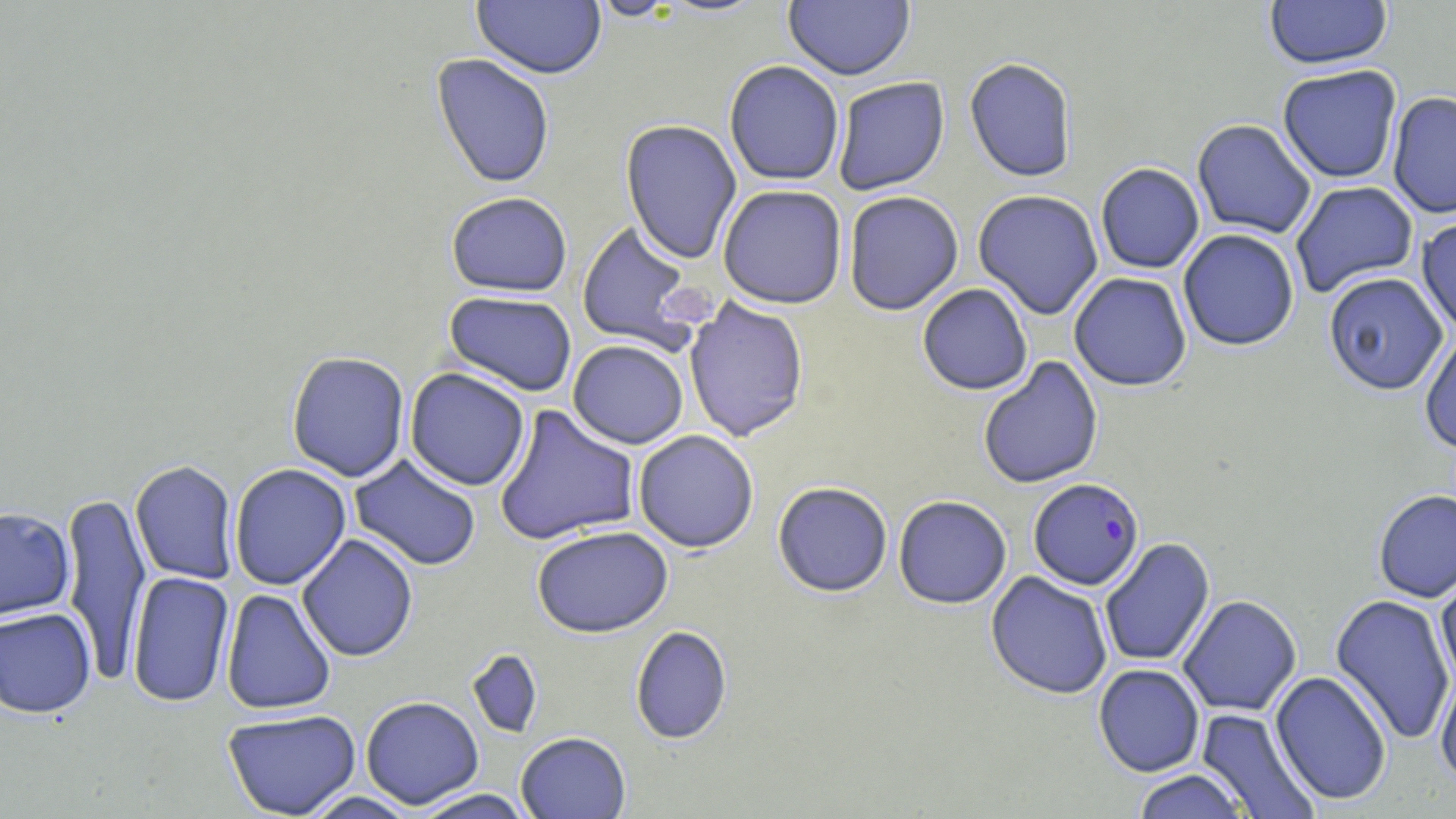

Summary:
  - Coordinate format: approximate bounding boxes as (x1, y1, x2, y2) in pixels
  - Uninfected red blood cell locations: (471, 0, 607, 79), (586, 0, 685, 21), (1264, 0, 1393, 71), (783, 1, 915, 81), (431, 53, 555, 189), (964, 57, 1078, 182), (724, 60, 845, 186), (1277, 64, 1403, 184), (832, 76, 950, 196), (1387, 90, 1456, 219), (620, 119, 742, 264), (1192, 119, 1317, 239), (1095, 162, 1205, 274), (1290, 180, 1419, 298), (717, 184, 847, 309), (972, 189, 1104, 319), (843, 191, 964, 315), (445, 192, 573, 297), (1416, 214, 1456, 338), (575, 221, 703, 354), (1177, 228, 1300, 351), (1323, 271, 1449, 396), (1068, 272, 1192, 392), (917, 283, 1033, 395), (443, 290, 578, 396), (683, 296, 810, 443), (1419, 332, 1456, 453), (568, 340, 689, 449), (286, 351, 410, 482), (977, 356, 1103, 490), (405, 368, 530, 491), (493, 404, 640, 546), (633, 430, 759, 553), (349, 454, 483, 571), (130, 460, 239, 585), (229, 463, 351, 590), (772, 482, 893, 597), (59, 489, 151, 683), (1373, 489, 1456, 602), (893, 495, 1012, 609), (0, 505, 75, 625), (532, 525, 673, 638), (296, 534, 419, 662), (1099, 537, 1215, 668), (1435, 569, 1456, 690), (985, 570, 1113, 699), (126, 571, 235, 708), (220, 588, 337, 715), (1177, 594, 1302, 716), (1329, 594, 1455, 744), (0, 607, 97, 718), (630, 625, 733, 744), (466, 649, 543, 739), (1093, 663, 1205, 777), (1435, 670, 1456, 788), (1270, 671, 1393, 806), (360, 695, 485, 810), (1196, 708, 1321, 818), (221, 709, 362, 819), (516, 731, 631, 819), (1130, 769, 1252, 818), (412, 788, 534, 818), (300, 790, 421, 819)
  - Plasmodium falciparum-infected red blood cell locations: (1028, 477, 1145, 591)
  - Slide-level diagnosis: Plasmodium falciparum
  - Modality: light microscopy
  - Magnification: 1000x
  - Image size: 1456×819 pixels
  - Field of view: one of a larger specimen
  - Stain: May-Grünwald-Giemsa
  - Preparation: thin blood smear